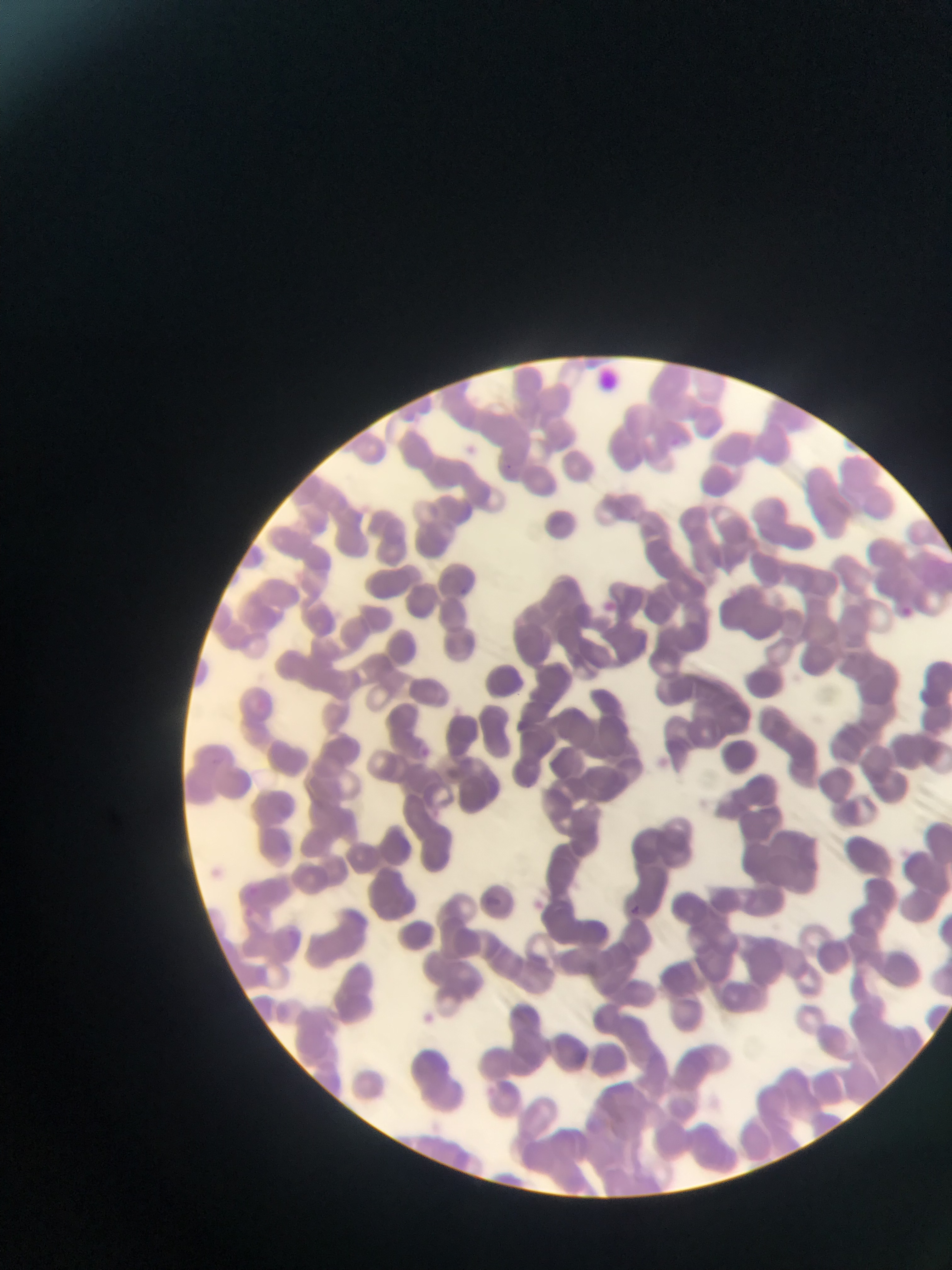

Approximate bounding boxes as {left, top, right, bottom} in pixels. Malaria parasite locations: {671, 437, 682, 448}, {503, 457, 518, 474}, {460, 581, 482, 605}, {601, 601, 619, 616}, {901, 605, 911, 618}, {416, 745, 431, 755}, {486, 891, 507, 912}, {631, 900, 643, 913}. Thin blood film. Collected in Ghana. Image is 952×1270 pixels. Mobile-phone photograph taken through the microscope. One field of view.